Locate and identify every blood parasite.
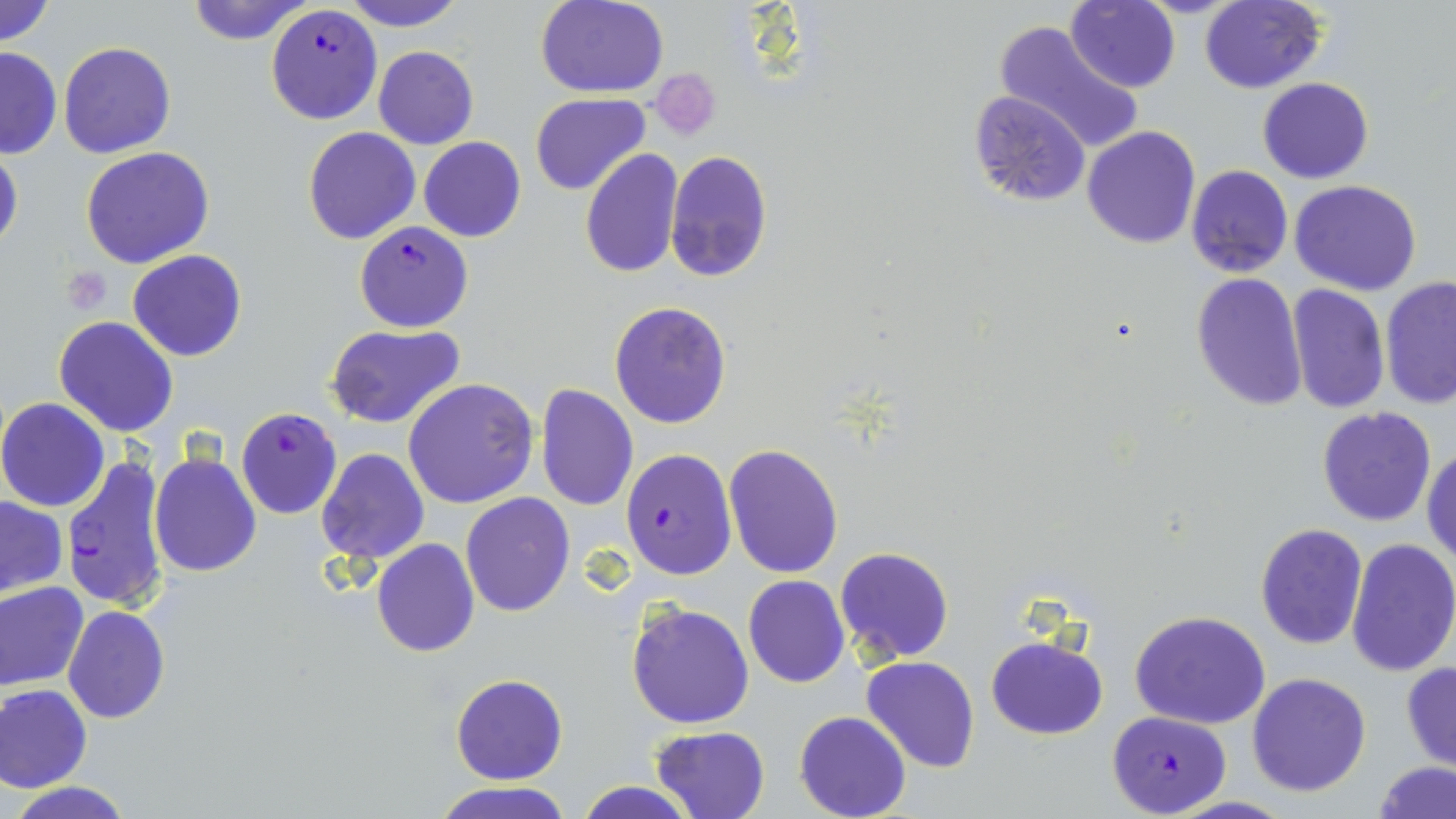
Approximate bounding boxes as [x1, y1, x2, y2] in pixels.
Plasmodium falciparum-infected red blood cells: [265, 4, 382, 125], [355, 219, 471, 330], [235, 407, 342, 520], [622, 447, 738, 581], [61, 451, 169, 615], [1106, 710, 1230, 817].
No Plasmodium ovale, Plasmodium malariae, Plasmodium vivax, Babesia divergens, or Trypanosoma brucei observed.

Platelet locations: [64, 266, 112, 312]. Uninfected red blood cell locations: [0, 0, 56, 48], [184, 0, 312, 46], [341, 0, 468, 30], [536, 0, 668, 97], [1199, 0, 1326, 94], [1066, 1, 1181, 93], [990, 18, 1142, 152], [58, 41, 176, 159], [372, 45, 478, 150], [0, 46, 63, 159], [648, 68, 721, 141], [1257, 77, 1374, 184], [968, 91, 1088, 205], [531, 93, 648, 194], [1082, 126, 1200, 248], [301, 127, 420, 246], [417, 138, 527, 242], [0, 142, 23, 258], [80, 146, 215, 268], [580, 149, 684, 279], [665, 150, 772, 283], [1187, 165, 1294, 278], [1290, 180, 1421, 296], [128, 250, 246, 362], [1191, 273, 1307, 411], [1379, 277, 1456, 411], [1286, 284, 1390, 412], [610, 301, 731, 429], [54, 317, 180, 438], [325, 322, 467, 430], [403, 378, 538, 508], [535, 383, 638, 512], [0, 397, 111, 511], [1316, 407, 1439, 528], [724, 443, 845, 579], [1424, 445, 1456, 568], [317, 448, 429, 565], [150, 452, 261, 576], [461, 492, 575, 616], [1, 496, 67, 596], [1255, 521, 1367, 649], [371, 538, 479, 657], [1346, 539, 1456, 677], [835, 546, 954, 664], [743, 576, 850, 689], [0, 581, 89, 691], [627, 600, 755, 730], [62, 606, 169, 724], [1130, 609, 1274, 730], [987, 635, 1109, 740], [861, 656, 981, 773], [1400, 660, 1456, 772], [1247, 672, 1372, 797], [450, 675, 567, 785], [1, 685, 92, 794], [794, 711, 910, 819], [649, 725, 770, 819], [1372, 760, 1455, 818], [573, 779, 701, 819], [433, 780, 572, 818], [4, 781, 136, 818]. Slide-level diagnosis: Plasmodium falciparum. May-Grünwald-Giemsa stain. Image is 1456×819 pixels. Single field of view. Thin blood film. Optical microscopy. 1000x magnification.